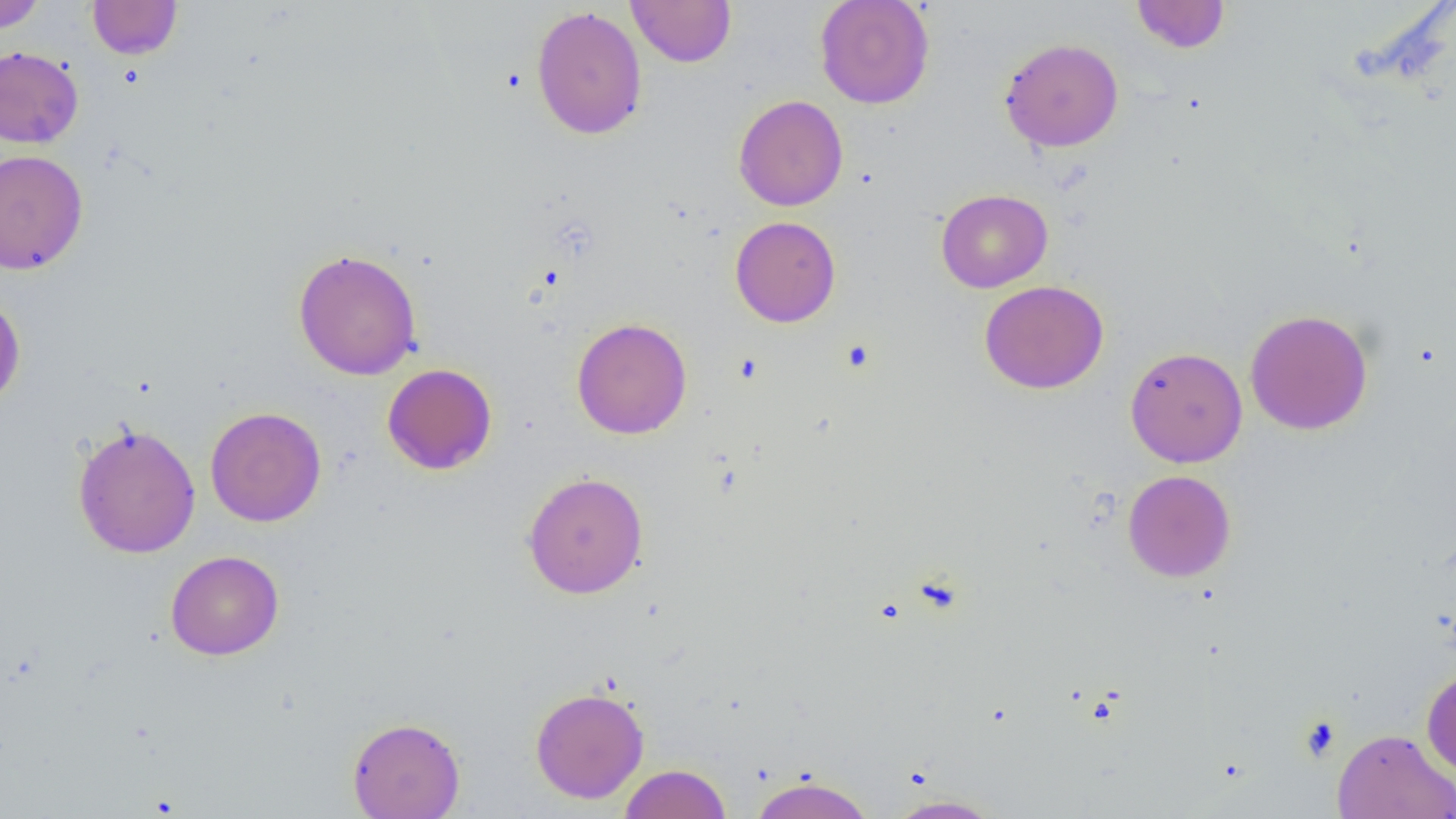
Approximate bounding boxes as (x1,y1)-(x2,y2) corner pairs in pixels. Uninfected red blood cell locations: (0,0)-(46,33), (87,0)-(182,59), (626,0)-(736,67), (815,0)-(935,109), (1131,0)-(1230,54), (531,6)-(647,140), (999,37)-(1124,152), (0,45)-(84,148), (733,95)-(848,212), (0,149)-(88,274), (936,188)-(1052,292), (730,216)-(841,327), (292,248)-(422,381), (979,280)-(1108,394), (0,292)-(26,413), (1245,309)-(1373,435), (571,317)-(692,439), (1125,347)-(1247,468), (382,363)-(498,475), (205,406)-(327,527), (72,422)-(201,558), (1122,469)-(1236,582), (522,472)-(649,599), (165,549)-(284,660), (1421,668)-(1456,778), (530,686)-(649,804), (347,716)-(465,818), (1332,728)-(1456,819), (619,763)-(731,819), (751,774)-(874,819), (885,794)-(1004,818). Platelet locations: (1298,715)-(1342,762). Slide-level diagnosis: negative for blood parasites. Optical microscopy. Thin blood smear. Single field of view. Image is 1456×819 pixels. Captured at 1000x magnification.